Locate every uninfected red blood cell.
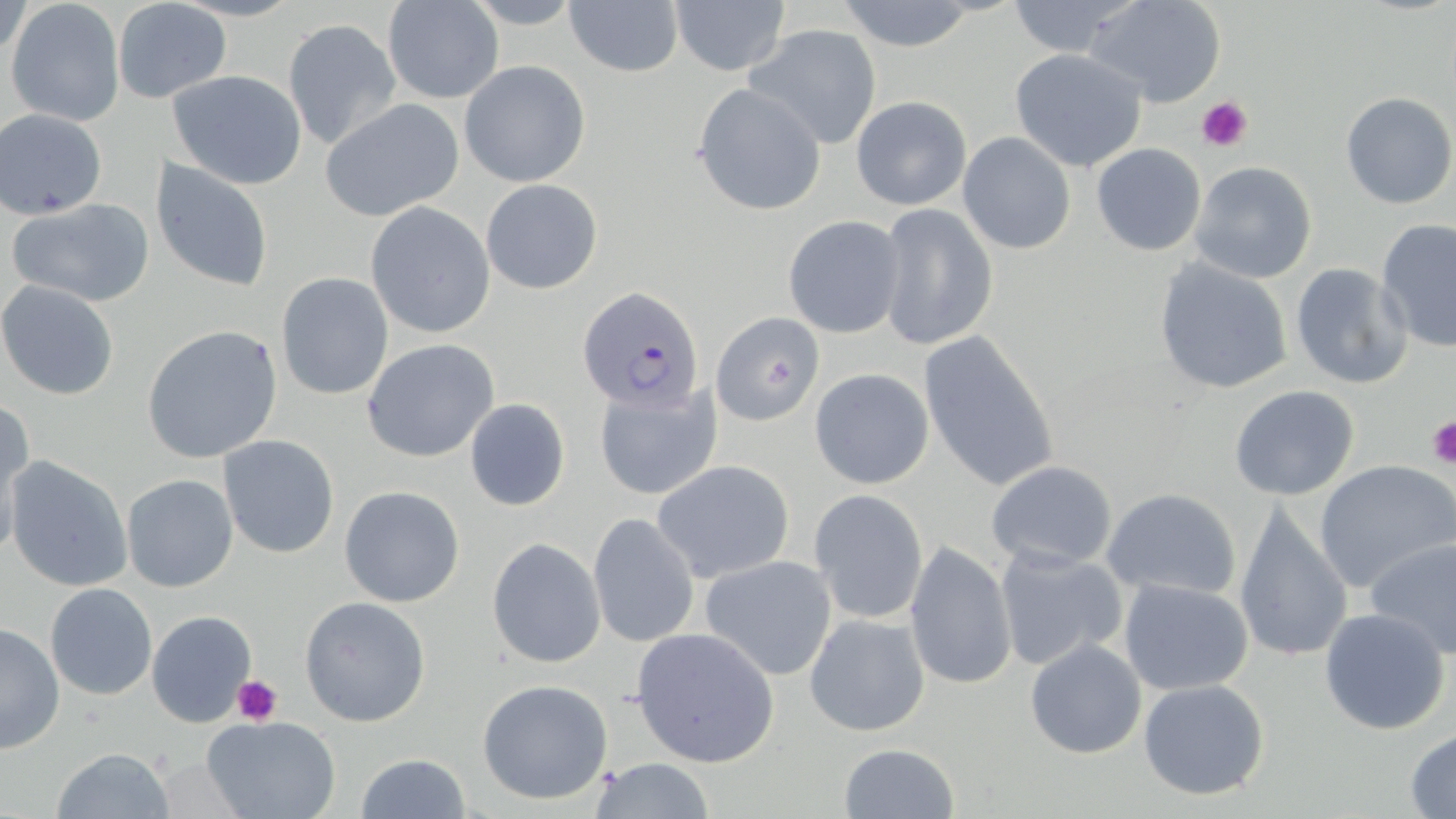
Approximate bounding boxes as named x1/y1/x2/y2 corners in pixels.
Uninfected red blood cells: (x1=5, y1=0, x2=126, y2=126), (x1=384, y1=0, x2=503, y2=103), (x1=563, y1=0, x2=684, y2=78), (x1=669, y1=0, x2=791, y2=76), (x1=1004, y1=0, x2=1141, y2=59), (x1=1086, y1=0, x2=1227, y2=108), (x1=834, y1=1, x2=984, y2=51), (x1=118, y1=3, x2=232, y2=104), (x1=284, y1=18, x2=402, y2=150), (x1=745, y1=23, x2=883, y2=150), (x1=1010, y1=49, x2=1149, y2=173), (x1=459, y1=60, x2=591, y2=188), (x1=168, y1=69, x2=308, y2=190), (x1=691, y1=83, x2=828, y2=216), (x1=1340, y1=91, x2=1455, y2=209), (x1=850, y1=95, x2=972, y2=210), (x1=319, y1=98, x2=466, y2=222), (x1=2, y1=109, x2=109, y2=219), (x1=957, y1=131, x2=1076, y2=255), (x1=1091, y1=143, x2=1207, y2=256), (x1=151, y1=158, x2=275, y2=293), (x1=1189, y1=162, x2=1318, y2=283), (x1=480, y1=178, x2=604, y2=295), (x1=7, y1=199, x2=153, y2=306), (x1=365, y1=203, x2=497, y2=339), (x1=875, y1=204, x2=998, y2=351), (x1=781, y1=215, x2=905, y2=338), (x1=1375, y1=218, x2=1456, y2=353), (x1=1152, y1=258, x2=1295, y2=395), (x1=1288, y1=262, x2=1413, y2=389), (x1=275, y1=272, x2=395, y2=400), (x1=1, y1=281, x2=119, y2=400), (x1=713, y1=311, x2=827, y2=425), (x1=141, y1=325, x2=284, y2=464), (x1=917, y1=330, x2=1060, y2=492), (x1=361, y1=340, x2=501, y2=463), (x1=809, y1=368, x2=934, y2=490), (x1=594, y1=383, x2=721, y2=501), (x1=1229, y1=384, x2=1359, y2=500), (x1=465, y1=398, x2=570, y2=511), (x1=1, y1=400, x2=35, y2=550), (x1=218, y1=435, x2=341, y2=558), (x1=5, y1=456, x2=133, y2=594), (x1=651, y1=459, x2=796, y2=582), (x1=983, y1=460, x2=1118, y2=570), (x1=1313, y1=460, x2=1456, y2=595), (x1=120, y1=474, x2=238, y2=593), (x1=339, y1=485, x2=466, y2=608), (x1=1102, y1=487, x2=1243, y2=601), (x1=808, y1=489, x2=928, y2=625), (x1=1234, y1=501, x2=1354, y2=665), (x1=588, y1=512, x2=701, y2=648), (x1=726, y1=515, x2=896, y2=655), (x1=1365, y1=536, x2=1456, y2=661), (x1=486, y1=537, x2=605, y2=668), (x1=903, y1=542, x2=1016, y2=692), (x1=992, y1=544, x2=1128, y2=673), (x1=697, y1=553, x2=841, y2=682), (x1=1118, y1=579, x2=1255, y2=695), (x1=44, y1=583, x2=159, y2=700), (x1=299, y1=595, x2=431, y2=727), (x1=1318, y1=606, x2=1452, y2=736), (x1=147, y1=611, x2=256, y2=727), (x1=804, y1=612, x2=930, y2=737), (x1=0, y1=623, x2=64, y2=755), (x1=630, y1=626, x2=781, y2=768), (x1=1024, y1=638, x2=1147, y2=758), (x1=1138, y1=677, x2=1271, y2=802), (x1=477, y1=679, x2=615, y2=805), (x1=202, y1=716, x2=342, y2=819), (x1=1405, y1=729, x2=1456, y2=816), (x1=837, y1=742, x2=958, y2=818), (x1=51, y1=747, x2=178, y2=818), (x1=356, y1=753, x2=470, y2=819), (x1=588, y1=757, x2=715, y2=817).

Platelet locations: (x1=1197, y1=95, x2=1253, y2=153), (x1=1427, y1=418, x2=1456, y2=466), (x1=233, y1=674, x2=283, y2=724). Plasmodium falciparum-infected red blood cell locations: (x1=580, y1=286, x2=705, y2=411). Slide-level diagnosis: Plasmodium falciparum. Thin blood smear. 1000x magnification. One field of a larger specimen. Image is 1456×819 pixels. May-Grünwald-Giemsa-stained preparation. Optical microscopy.